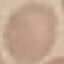
Result: negative for malaria parasites. Thin blood smear. Cell patch, automatically extracted from a larger field of view and resized to 64 × 64 pixels. Photographed with a smartphone camera at the microscope eyepiece. Giemsa-stained preparation.